Report the malaria status of this cell.
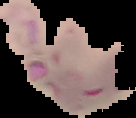

It is parasitized.

Summary:
  - Image type: cell region segmented out of the field of view; surrounding area masked to black
  - Preparation: thin blood smear
  - Image size: 136×118 pixels